Assess this cell for malaria.
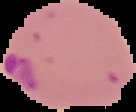

It is parasitized.

image type = segmented cell region on a black background
image size = 136×112 pixels
preparation = thin blood film